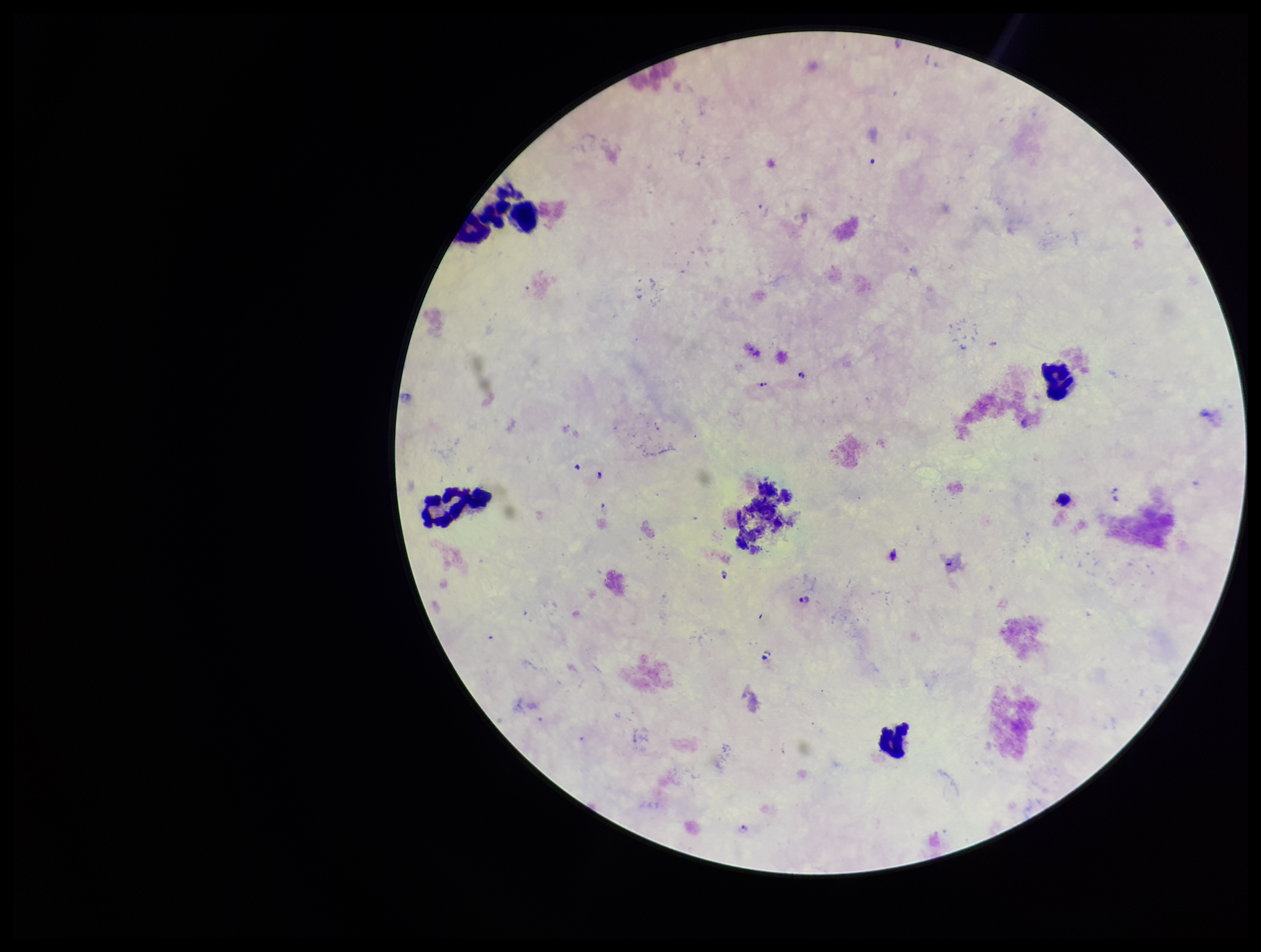

Patient malaria status: positive. Parasite count: 2. Giemsa stain. Plasmodium parasites: seen. One field from this slide. Photographed through the microscope eyepiece with a smartphone camera. Preparation: thick smear. Leukocyte count: 5. Species reported for this patient: Plasmodium falciparum. Image is 1261×952 pixels.